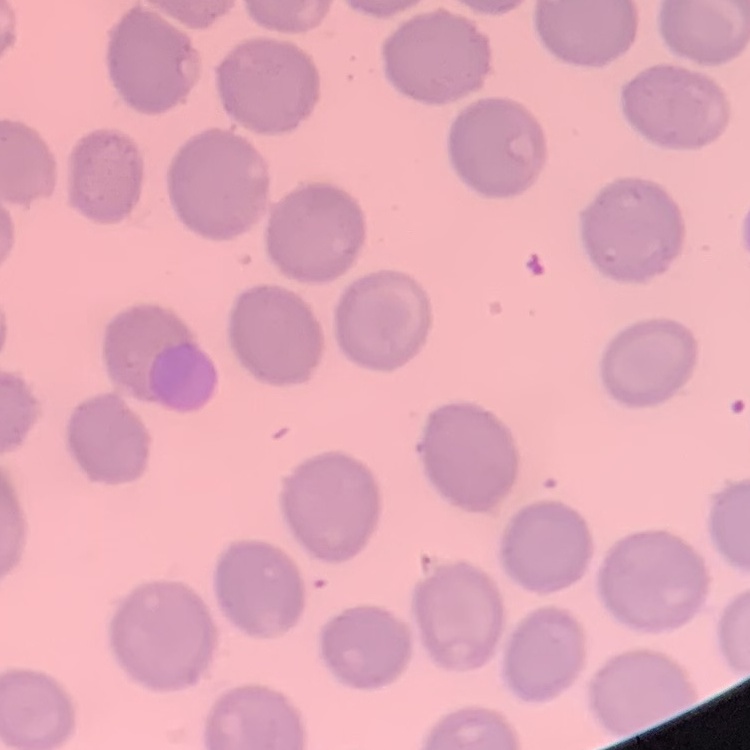

erythrocyte morphology = no rouleaux formation
image type = square crop of a larger photomicrograph
stain = Field's or Giemsa
preparation = thin peripheral smear